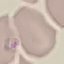
Summary:
  - Result: malaria parasites detected
  - Capture: smartphone camera at the microscope eyepiece
  - Stain: Giemsa
  - Image type: cell patch, automatically extracted from a larger field of view and resized to 64 × 64 pixels
  - Preparation: thin blood film